Assess this cell for malaria.
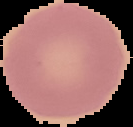

Uninfected.

Cell region segmented out of the field of view; the surrounding area is masked to black. From a thin blood smear. Image is 133×127 pixels.